Outline each Plasmodium malariae-infected red blood cell.
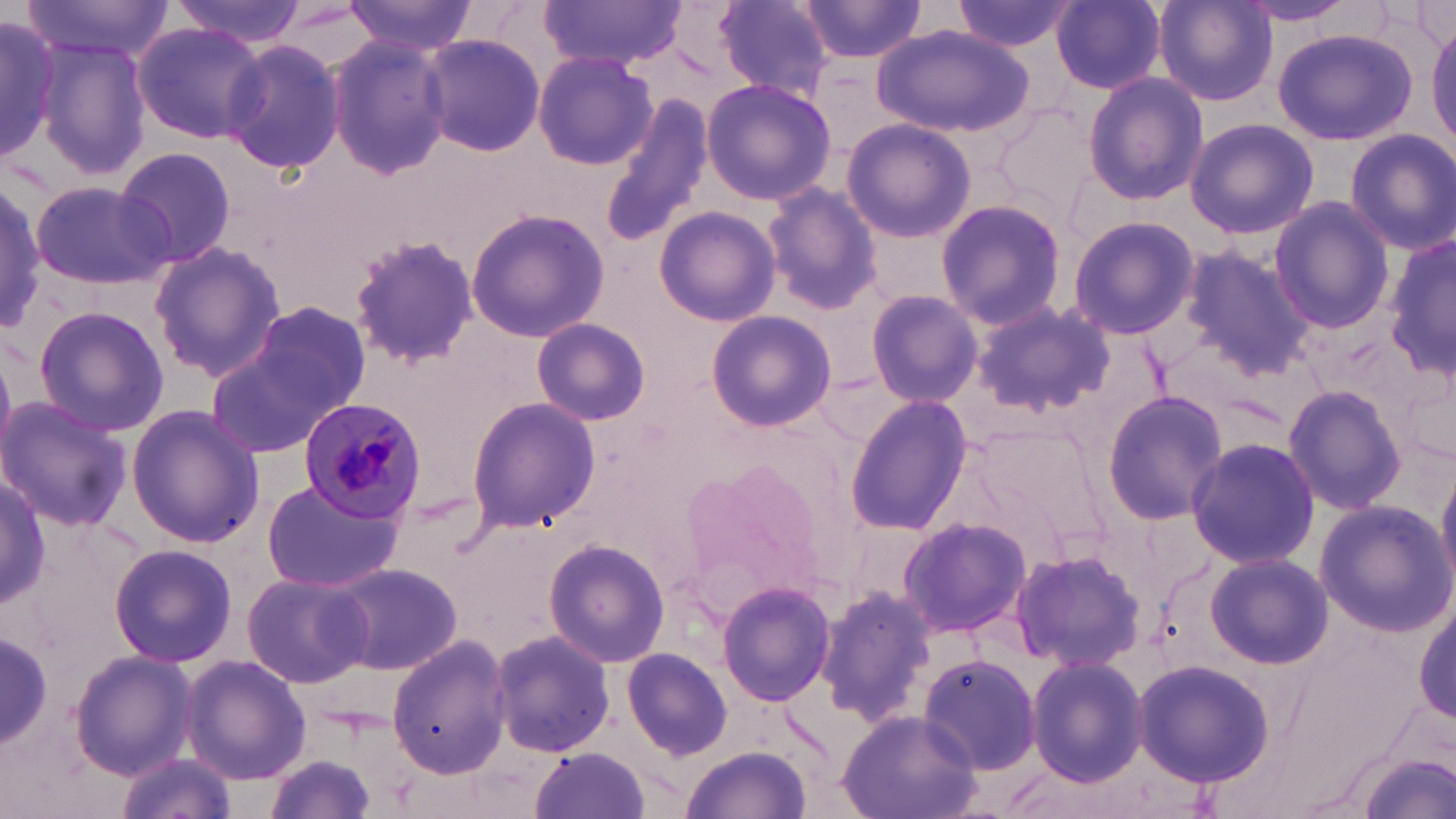
Approximate bounding boxes as (x1,y1)-(x2,y2) corner pairs in pixels.
Plasmodium malariae-infected red blood cells: (300,400)-(429,520).

{
  "slide_level_diagnosis": "Plasmodium malariae",
  "magnification": "1000x",
  "field_of_view": "single",
  "uninfected_red_blood_cell_locations": "approximate bounding boxes as (x1,y1)-(x2,y2) corner pairs in pixels: (21,0)-(173,62), (170,0)-(308,45), (343,0)-(479,54), (537,0)-(691,69), (712,0)-(837,99), (796,0)-(928,65), (951,0)-(1077,54), (1052,0)-(1166,93), (1153,1)-(1278,108), (1237,1)-(1359,25), (0,11)-(67,163), (1429,20)-(1456,151), (131,22)-(266,144), (872,23)-(1033,136), (1270,27)-(1420,147), (418,33)-(547,157), (36,36)-(154,181), (325,36)-(454,179), (220,40)-(345,175), (532,51)-(660,171), (1082,71)-(1208,206), (701,79)-(837,206), (601,92)-(717,248), (996,103)-(1100,213), (842,117)-(977,243), (1184,118)-(1318,240), (1346,129)-(1456,254), (112,146)-(237,269), (31,179)-(173,292), (0,184)-(49,323), (762,184)-(883,315), (1268,197)-(1393,335), (936,198)-(1066,328), (464,204)-(610,343), (654,207)-(780,327), (1068,216)-(1200,339), (1388,233)-(1455,383), (346,236)-(479,368), (150,241)-(286,380), (1178,247)-(1317,377), (866,288)-(982,407), (242,296)-(373,425), (970,299)-(1113,417), (31,304)-(170,437), (705,310)-(838,432), (531,316)-(651,427), (205,326)-(358,461), (1281,384)-(1407,517), (1101,390)-(1229,524), (465,395)-(600,534), (845,395)-(976,536), (0,397)-(131,530), (126,405)-(264,547), (970,421)-(1099,535), (1185,437)-(1318,569), (677,454)-(833,611), (1436,463)-(1456,593), (1,473)-(49,607), (260,477)-(404,594), (1314,499)-(1453,636), (897,516)-(1030,638), (543,538)-(670,668), (110,542)-(237,668), (1009,548)-(1146,674), (1205,551)-(1332,669), (325,562)-(463,675), (241,571)-(371,688), (717,580)-(837,708), (817,583)-(939,725), (1415,607)-(1454,727), (2,628)-(52,753), (490,628)-(619,758), (385,636)-(511,779), (623,647)-(733,760), (69,651)-(194,777), (917,654)-(1044,776), (182,655)-(311,785), (1025,655)-(1147,786), (1131,658)-(1276,788), (836,708)-(983,819), (682,745)-(814,818), (529,747)-(653,819), (1355,750)-(1455,819), (114,752)-(236,819), (261,753)-(378,819)",
  "stain": "May-Grünwald-Giemsa",
  "preparation": "thin blood film",
  "modality": "light microscopy",
  "image_size": "1456×819 pixels"
}